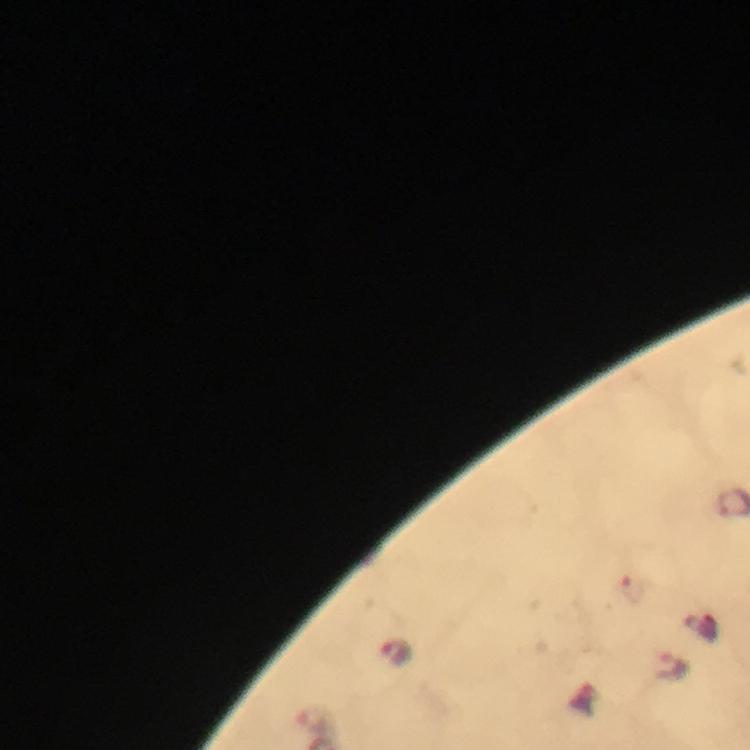

Approximate object centers, in pixels from the top-left corner.
Summary:
  - Malaria parasite locations: (x=395, y=652), (x=671, y=666), (x=314, y=718)
  - Magnification: 100x
  - Stain: Giemsa
  - Immersion oil: applied
  - Preparation: thick blood smear
  - Capture: smartphone camera through the microscope
  - Image size: 750×750 pixels
  - Context: from a malaria diagnostic workup
  - Cropped from: a single field of view